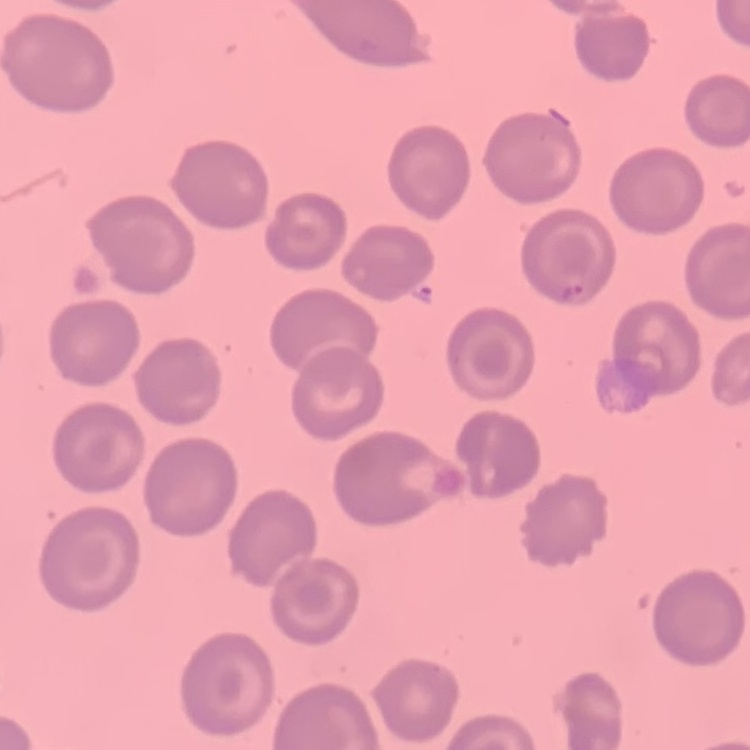

{
  "red_blood_cell_morphology": "no rouleaux formation",
  "stain": "Field's or Giemsa",
  "preparation": "thin blood smear",
  "image_type": "square crop of a larger photomicrograph"
}